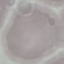

Summary:
  - Malaria status: uninfected
  - Capture: smartphone camera at the microscope eyepiece
  - Preparation: thin blood film
  - Image type: cell patch, automatically extracted from a larger field of view and resized to 64 × 64 pixels
  - Stain: Giemsa